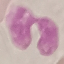
Result: negative for malaria parasites. Acquired by smartphone through the microscope eyepiece. Cell patch, automatically extracted from a larger field of view and resized to 64 × 64 pixels. Thin blood film. Giemsa-stained preparation.